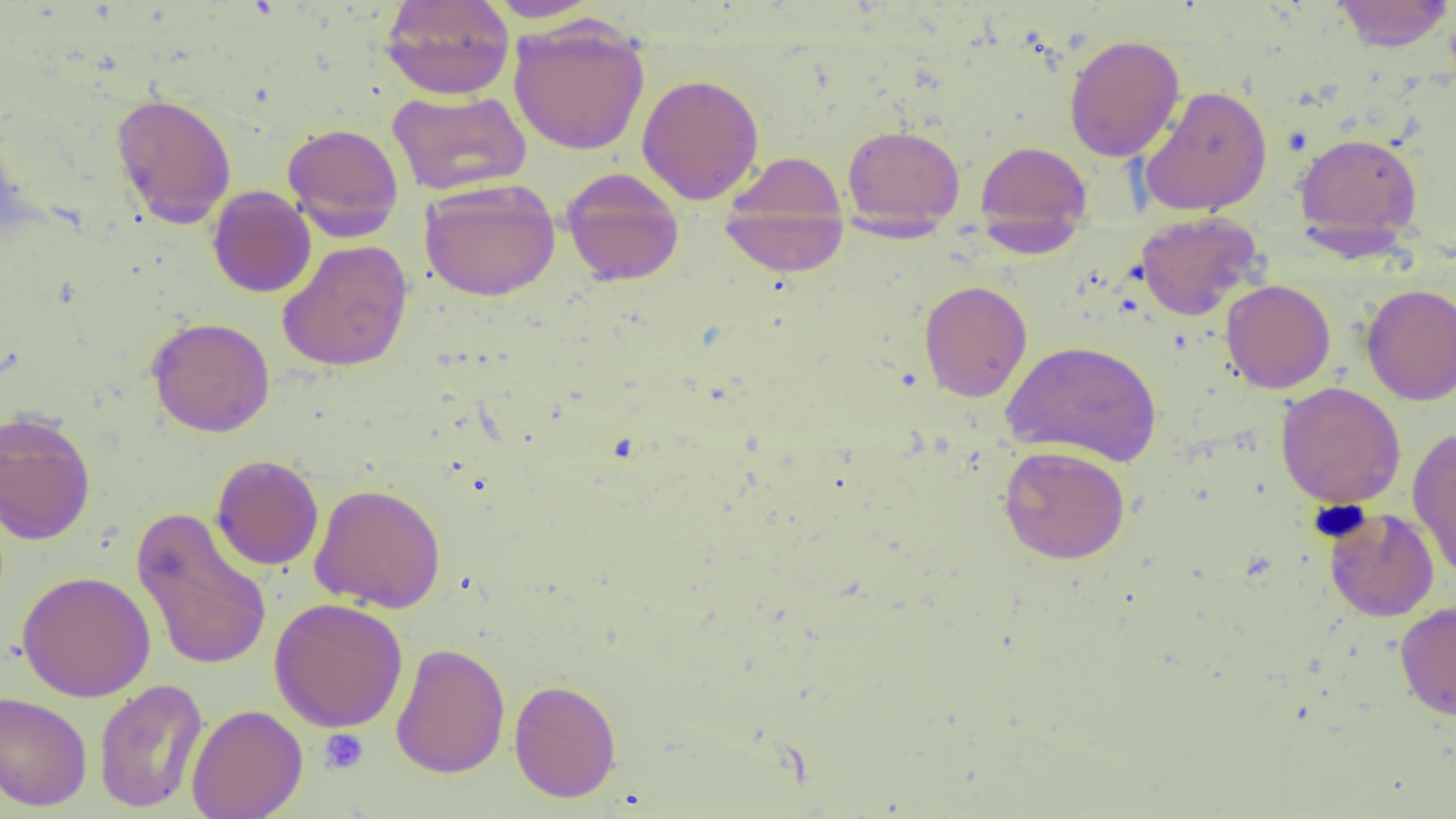
Approximate bounding boxes as (x1,y1)-(x2,y2) corner pairs in pixels. Platelet locations: (319,728)-(369,775). Uninfected red blood cell locations: (379,0)-(515,100), (484,0)-(602,23), (1330,0)-(1455,52), (507,18)-(650,156), (1064,34)-(1185,162), (636,73)-(764,204), (1139,85)-(1273,216), (387,89)-(532,196), (110,92)-(237,227), (0,118)-(36,245), (282,122)-(404,239), (841,124)-(965,230), (1294,132)-(1423,245), (974,140)-(1093,247), (724,151)-(848,244), (561,168)-(685,287), (419,178)-(561,302), (207,186)-(316,298), (719,192)-(848,277), (1135,211)-(1262,321), (277,240)-(413,372), (918,279)-(1033,402), (1221,279)-(1336,393), (1361,284)-(1456,406), (147,317)-(275,437), (1002,340)-(1162,468), (1276,381)-(1406,508), (0,409)-(97,545), (1407,425)-(1456,582), (998,444)-(1130,564), (211,454)-(324,571), (309,483)-(447,613), (131,506)-(272,672), (1324,507)-(1440,622), (16,571)-(156,702), (269,597)-(408,733), (1395,600)-(1456,721), (391,642)-(510,779), (93,678)-(208,813), (509,679)-(621,802), (0,690)-(92,812), (187,704)-(308,819). Slide-level diagnosis: negative for blood parasites. One field of a larger specimen. Thin blood smear. Image is 1456×819 pixels. 1000x magnification. Light microscopy.